Locate every blood parasite and identify its species.
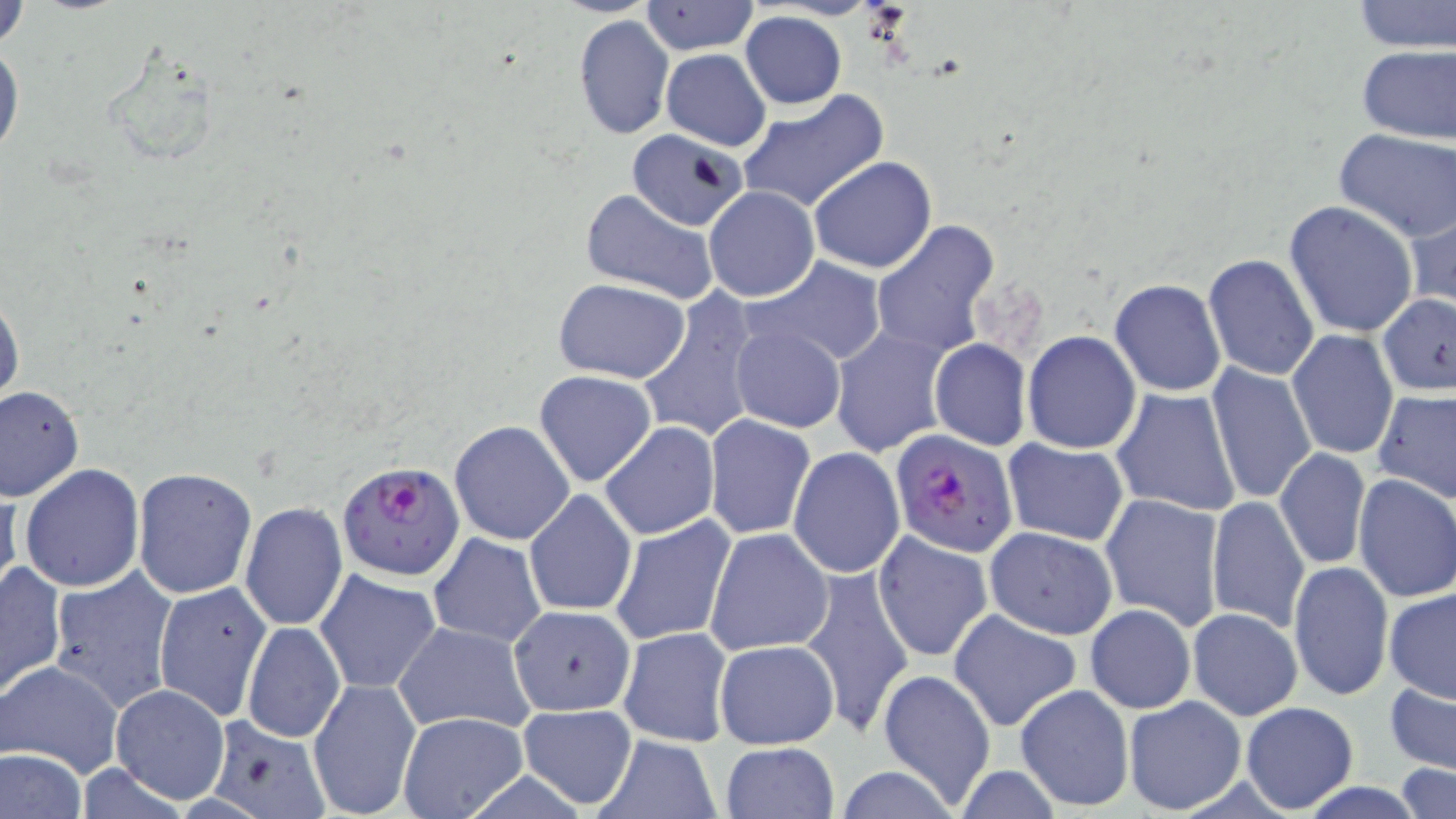

Approximate bounding boxes as (x1, y1, x2, y2) in pixels.
Plasmodium falciparum-infected red blood cells: (893, 429, 1018, 557), (336, 460, 466, 582).
No Plasmodium ovale, Plasmodium malariae, Plasmodium vivax, Babesia divergens, or Trypanosoma brucei observed.

Uninfected red blood cell locations: (1350, 0, 1456, 53), (2, 1, 29, 56), (640, 1, 759, 55), (740, 11, 847, 109), (575, 14, 675, 140), (0, 37, 22, 160), (1356, 44, 1456, 145), (661, 48, 770, 151), (98, 50, 220, 170), (737, 90, 888, 216), (627, 129, 745, 232), (1334, 129, 1456, 240), (809, 156, 937, 273), (704, 186, 819, 303), (580, 190, 720, 306), (1283, 200, 1419, 338), (1405, 201, 1455, 318), (871, 222, 998, 360), (1203, 254, 1320, 380), (746, 255, 889, 370), (1109, 277, 1227, 396), (552, 278, 692, 384), (636, 287, 765, 445), (1377, 294, 1456, 395), (0, 295, 23, 411), (729, 323, 847, 432), (830, 327, 951, 458), (1023, 330, 1142, 454), (1287, 330, 1398, 460), (929, 339, 1031, 451), (1207, 364, 1319, 507), (533, 370, 657, 488), (0, 385, 83, 502), (1373, 387, 1456, 503), (1111, 388, 1241, 517), (704, 413, 815, 540), (450, 420, 575, 545), (599, 421, 720, 541), (1002, 438, 1129, 547), (1276, 446, 1372, 570), (789, 447, 904, 578), (19, 464, 145, 592), (131, 467, 258, 598), (1352, 475, 1456, 603), (0, 482, 24, 602), (524, 488, 636, 616), (1101, 493, 1224, 630), (1206, 495, 1309, 633), (239, 502, 348, 632), (610, 515, 737, 646), (985, 525, 1117, 639), (705, 528, 833, 655), (874, 532, 993, 661), (428, 533, 547, 647), (0, 561, 66, 700), (1289, 561, 1393, 701), (48, 565, 181, 715), (804, 567, 913, 742), (314, 568, 443, 693), (154, 581, 272, 724), (1384, 587, 1456, 704), (1085, 603, 1196, 714), (510, 604, 636, 715), (949, 608, 1082, 732), (1188, 608, 1302, 719), (393, 620, 536, 736), (242, 621, 345, 743), (617, 627, 732, 747), (894, 628, 1042, 774), (713, 638, 839, 749), (1, 658, 124, 777), (879, 669, 997, 808), (306, 676, 423, 819), (1384, 680, 1456, 776), (1014, 683, 1134, 811), (111, 685, 229, 802), (1123, 695, 1246, 815), (1240, 701, 1359, 813), (515, 704, 640, 811), (396, 711, 528, 819), (202, 718, 332, 819), (591, 733, 724, 819), (719, 742, 838, 819), (0, 748, 88, 819), (1393, 763, 1456, 818), (829, 765, 968, 819). Slide-level diagnosis: Plasmodium falciparum. Image is 1456×819 pixels. Thin blood film. One field of a larger specimen. 1000x magnification. May-Grünwald-Giemsa stain. Optical microscopy.